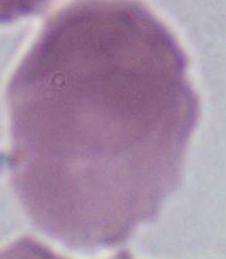

A red blood cell is shown. 1000x magnification. Photomicrograph.